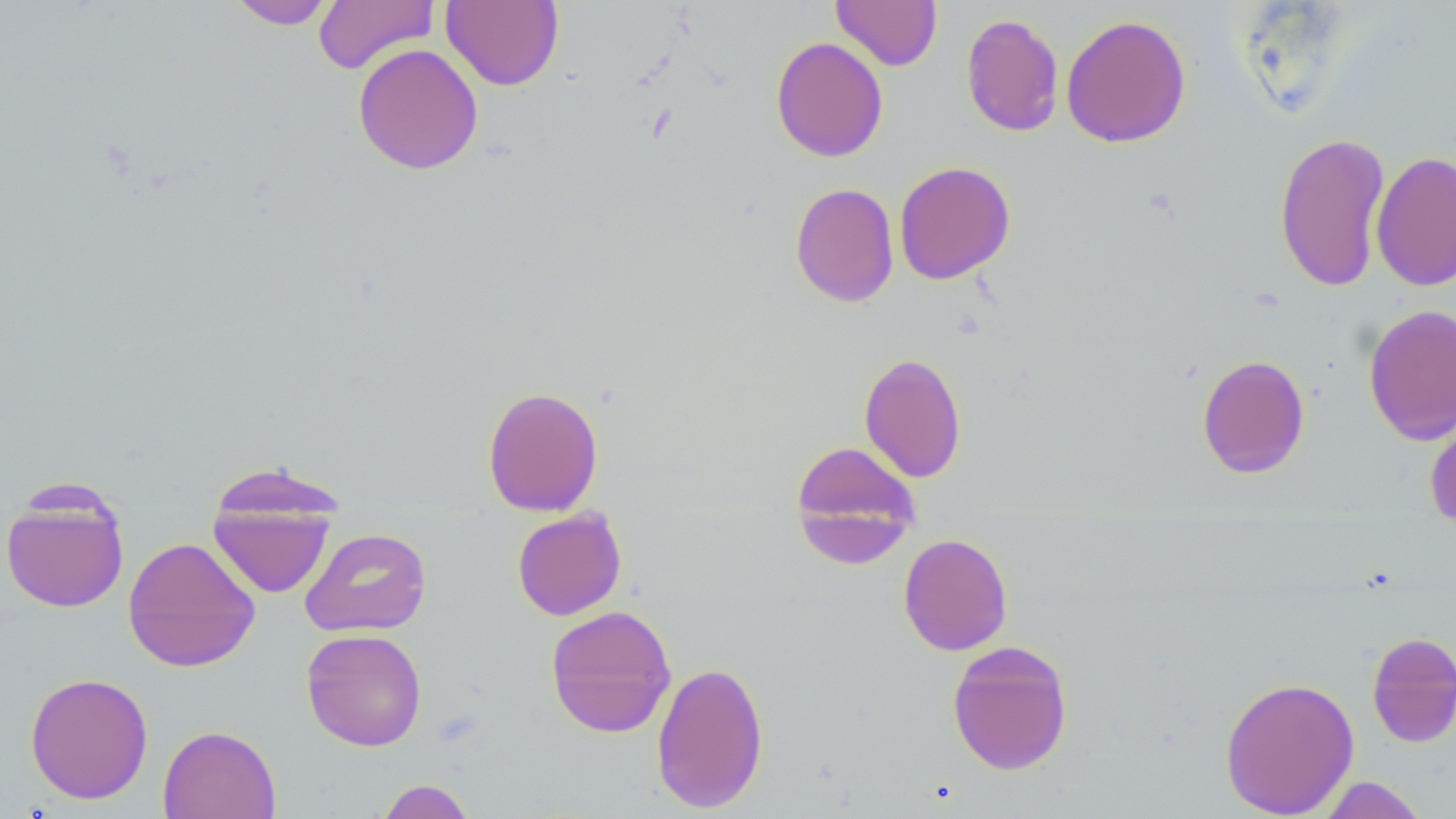

slide-level diagnosis = no evidence of blood parasites
stain = May-Grünwald-Giemsa
preparation = thin blood smear
modality = optical microscopy
image size = 1456×819 pixels
magnification = 1000x
field of view = one of a larger specimen
uninfected red blood cell locations = approximate bounding boxes as [x1, y1, x2, y2] in pixels: [228, 0, 337, 29], [313, 0, 439, 74], [441, 0, 564, 90], [831, 0, 942, 70], [961, 13, 1064, 137], [1061, 14, 1191, 148], [770, 36, 888, 162], [352, 43, 484, 175], [1273, 131, 1391, 293], [1370, 150, 1456, 292], [893, 160, 1016, 285], [789, 182, 900, 308], [1363, 304, 1456, 446], [859, 352, 967, 483], [1196, 354, 1310, 479], [482, 386, 603, 516], [1424, 405, 1456, 533], [789, 439, 921, 568], [1, 484, 130, 614], [207, 496, 336, 599], [511, 507, 627, 621], [300, 527, 432, 637], [898, 533, 1013, 656], [123, 536, 261, 672], [545, 604, 676, 738], [301, 628, 427, 751], [1366, 631, 1456, 747], [946, 640, 1073, 776], [651, 660, 769, 813], [24, 672, 154, 805], [1219, 675, 1360, 818], [158, 724, 281, 819], [1314, 776, 1429, 818], [376, 779, 477, 819]